State which parasite is depicted.
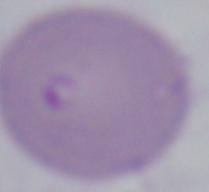
This is Babesia.

Micrograph. 1000x magnification.